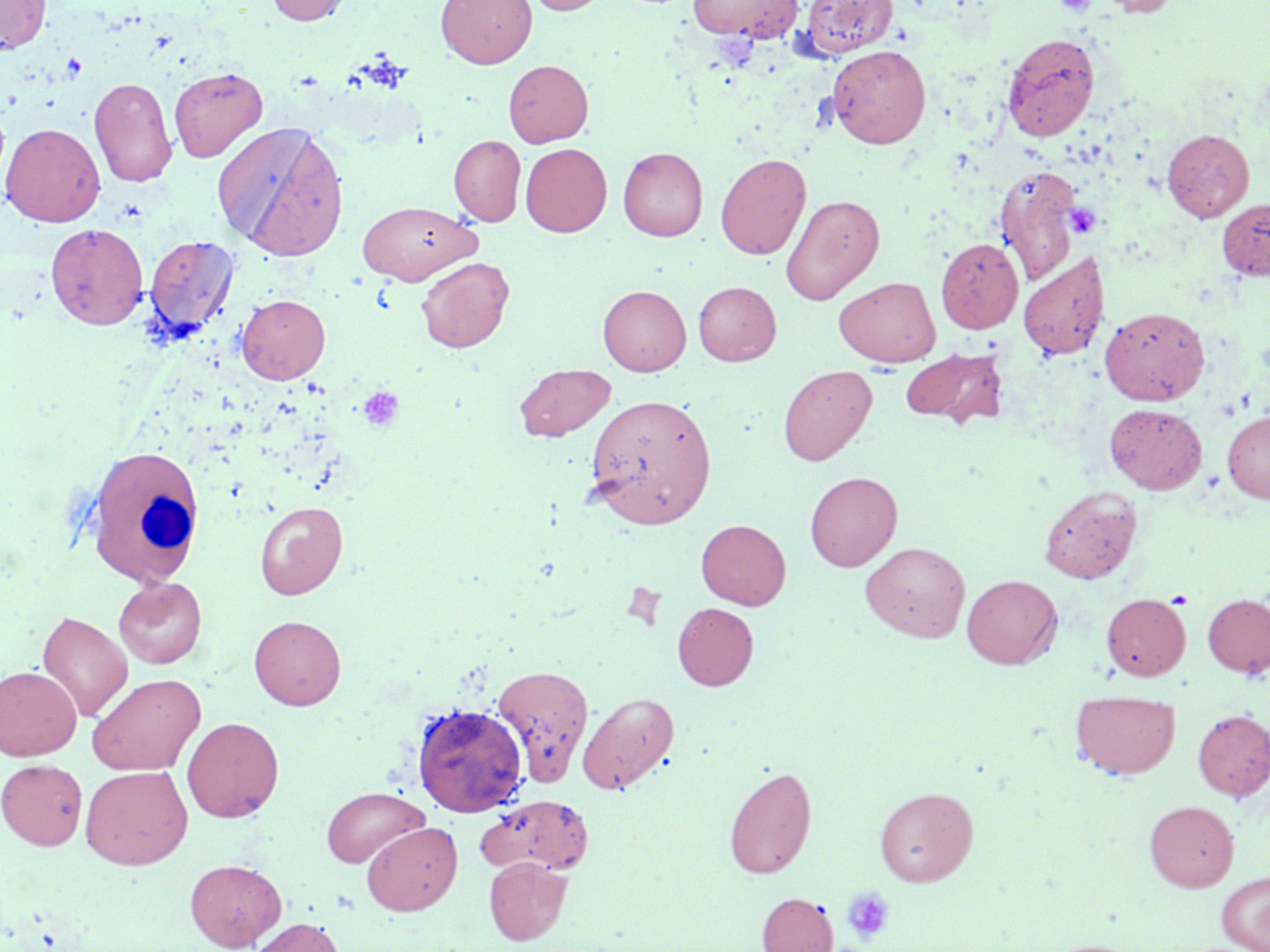 Approximate bounding boxes as (x1, y1, x2, y2) in pixels. Platelet locations: (1054, 0, 1096, 16), (1065, 203, 1100, 237), (357, 386, 405, 433), (841, 887, 895, 944). White blood cell locations: (83, 444, 206, 587). Uninfected red blood cell locations: (0, 0, 51, 54), (266, 0, 353, 25), (436, 0, 536, 68), (526, 0, 610, 15), (688, 0, 802, 42), (800, 0, 897, 58), (1095, 0, 1182, 17), (1001, 32, 1099, 141), (827, 44, 931, 148), (503, 60, 593, 147), (169, 67, 267, 163), (89, 76, 177, 186), (213, 121, 348, 261), (1, 123, 105, 227), (1162, 129, 1254, 222), (449, 134, 526, 226), (520, 143, 612, 237), (618, 147, 707, 241), (715, 153, 810, 260), (995, 165, 1083, 285), (780, 194, 884, 305), (1217, 198, 1270, 280), (356, 200, 481, 285), (45, 223, 148, 330), (144, 234, 240, 342), (935, 238, 1023, 334), (1018, 251, 1109, 360), (416, 257, 514, 353), (835, 276, 940, 367), (693, 281, 781, 365), (598, 285, 691, 375), (235, 294, 330, 384), (1100, 305, 1209, 405), (901, 348, 1007, 429), (514, 363, 615, 441), (778, 364, 877, 466), (583, 393, 717, 528), (1104, 403, 1207, 494), (1222, 410, 1270, 503), (805, 471, 902, 571), (1039, 484, 1142, 584), (254, 500, 348, 600), (696, 519, 790, 609), (861, 541, 970, 642), (962, 574, 1062, 669), (113, 576, 207, 668), (1101, 593, 1190, 680), (1202, 593, 1270, 678), (672, 602, 758, 690), (37, 610, 133, 722), (249, 615, 346, 709), (491, 663, 594, 786), (0, 666, 82, 760), (87, 673, 205, 776), (1070, 690, 1180, 778), (577, 691, 679, 794), (412, 702, 527, 817), (1192, 708, 1270, 800), (182, 716, 284, 822), (1, 759, 88, 850), (80, 765, 192, 869), (724, 765, 817, 879), (321, 786, 428, 868), (874, 786, 978, 886), (476, 794, 594, 876), (1145, 800, 1239, 891), (362, 821, 461, 915), (483, 857, 571, 945), (184, 858, 286, 951), (1216, 872, 1270, 951), (756, 892, 838, 952), (247, 917, 345, 952). Slide-level diagnosis: negative for blood parasites. May-Grünwald-Giemsa stain. Image is 1270×952 pixels. Light microscopy. Single field of view. Thin blood smear. Captured at 1000x magnification.